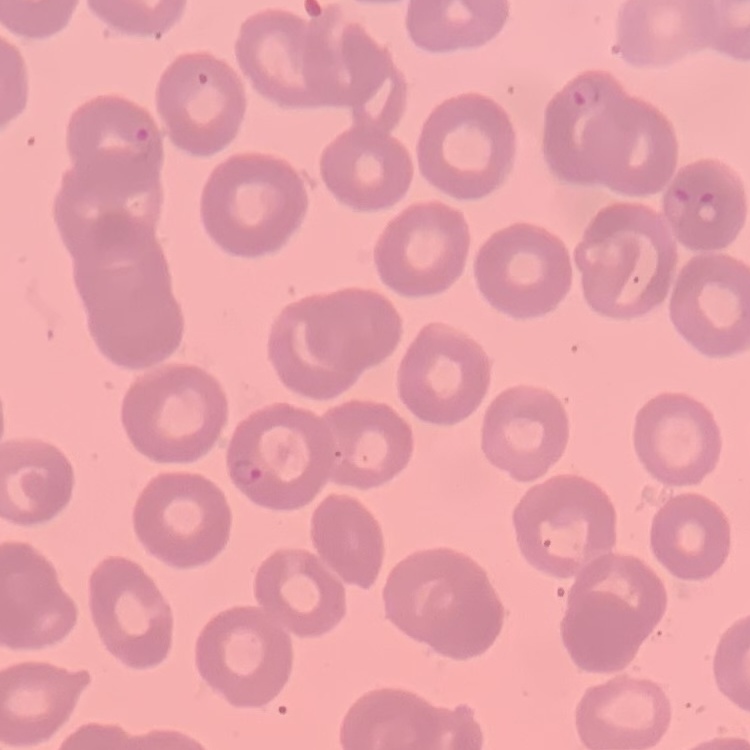

The red blood cells exhibit no rouleaux formation. One tile cut from a larger photomicrograph. Stained with either Field's or Giemsa. Thin blood smear.